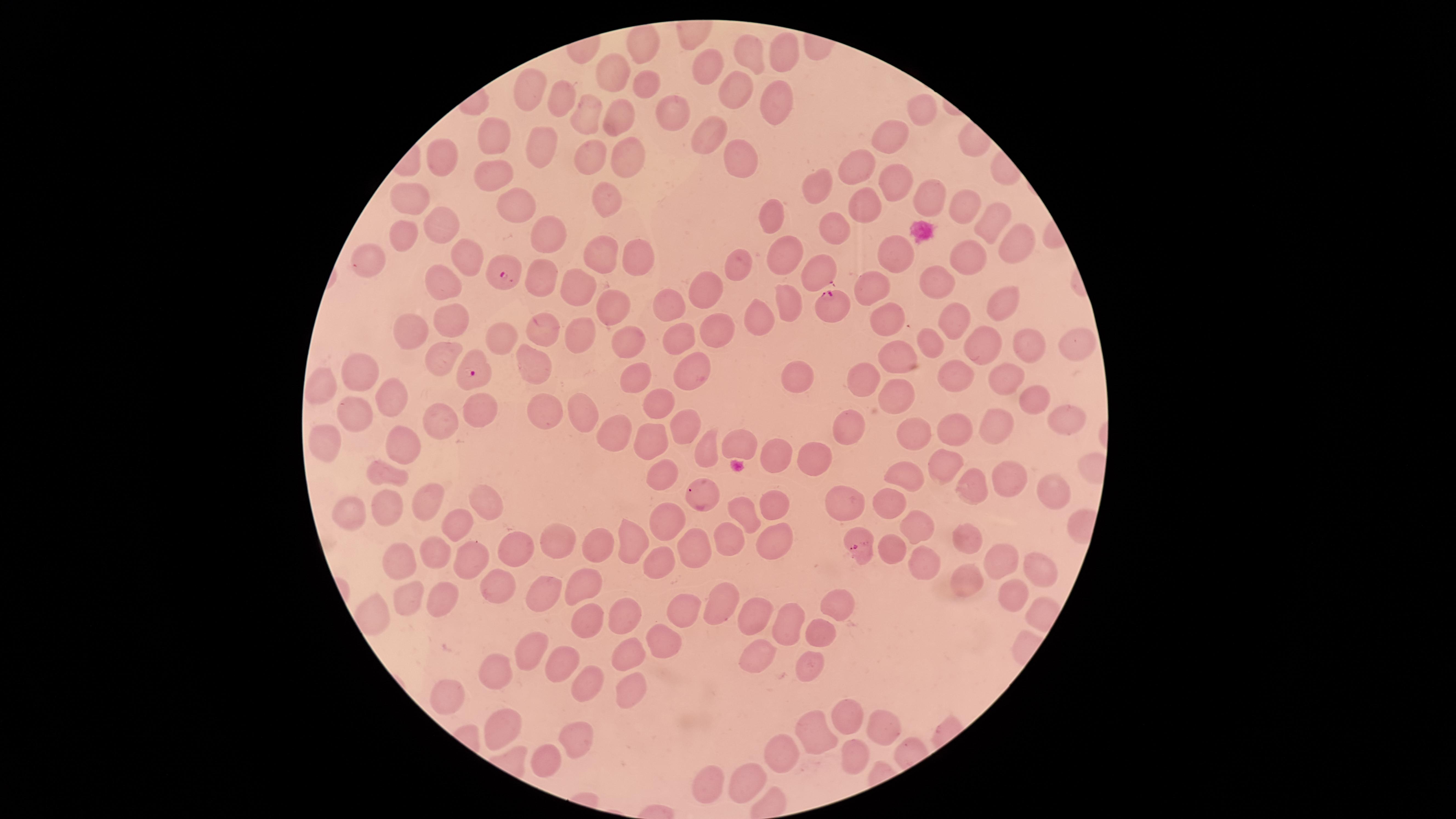 Approximate marker points as (x, y) in pixels. Uninfected red blood cells: (642, 41), (751, 48), (785, 52), (711, 62), (616, 70), (643, 83), (734, 87), (528, 88), (560, 94), (774, 100), (926, 106), (588, 107), (618, 115), (667, 115), (496, 130), (710, 134), (893, 134), (539, 140), (440, 155), (622, 155), (585, 156), (739, 161), (860, 161), (494, 176), (896, 176), (818, 189), (930, 194), (411, 195), (610, 199), (864, 200), (512, 202), (961, 203), (774, 213), (991, 220), (445, 221), (550, 228), (826, 228), (406, 232), (1014, 245), (597, 248), (781, 252), (368, 254), (467, 254), (636, 254), (899, 256), (971, 256), (738, 265), (813, 271), (939, 275), (539, 277), (875, 282), (443, 284), (709, 286), (581, 291), (666, 300), (998, 300), (789, 301), (610, 308), (953, 314), (760, 317), (453, 318), (886, 319), (676, 327), (542, 328), (716, 329), (409, 331), (501, 334), (577, 334), (930, 338), (991, 339), (1069, 340), (627, 341), (1034, 343), (901, 355), (443, 358), (530, 359), (356, 365), (689, 368), (951, 369), (866, 375), (1005, 376), (793, 377), (633, 378), (388, 385), (324, 386), (889, 395), (1037, 397), (656, 398), (484, 408), (354, 409), (579, 410), (548, 413), (1060, 417), (438, 419), (678, 423), (845, 426), (953, 427), (1000, 428), (912, 432), (617, 435), (645, 442), (737, 443), (323, 445), (394, 447), (705, 449), (813, 455), (774, 456), (942, 461), (387, 472), (903, 472), (660, 473), (1005, 473), (1050, 484), (966, 488), (430, 497), (886, 497), (694, 498), (772, 499), (844, 501), (486, 502), (386, 508), (354, 509), (747, 513), (666, 517), (919, 522), (456, 523), (772, 529), (633, 534), (557, 536), (970, 536), (727, 537), (695, 545), (514, 546), (592, 549), (469, 550), (395, 556), (435, 557), (1006, 558), (660, 560), (919, 560), (1039, 564), (495, 579), (586, 580), (967, 580), (541, 594), (1007, 595), (409, 598), (444, 601), (723, 603), (679, 609), (835, 609), (625, 615), (750, 617), (582, 620), (793, 624), (823, 638), (661, 640), (529, 650), (764, 652), (625, 653), (567, 661), (809, 667), (498, 679), (584, 689), (442, 696), (628, 696), (851, 715), (500, 721), (882, 726), (816, 733), (575, 739), (782, 754), (856, 758), (545, 762), (751, 780), (710, 788). Parasitized red blood cells: (508, 271), (833, 306), (472, 372), (859, 546). The visible region is circular. Giemsa-stained preparation. Species: Plasmodium falciparum. Thin blood film. Presence: malaria parasites detected. Image is 1456×819 pixels. Smartphone photograph through the microscope eyepiece. One field of view of the specimen.